Comment on the morphology of the red blood cells.
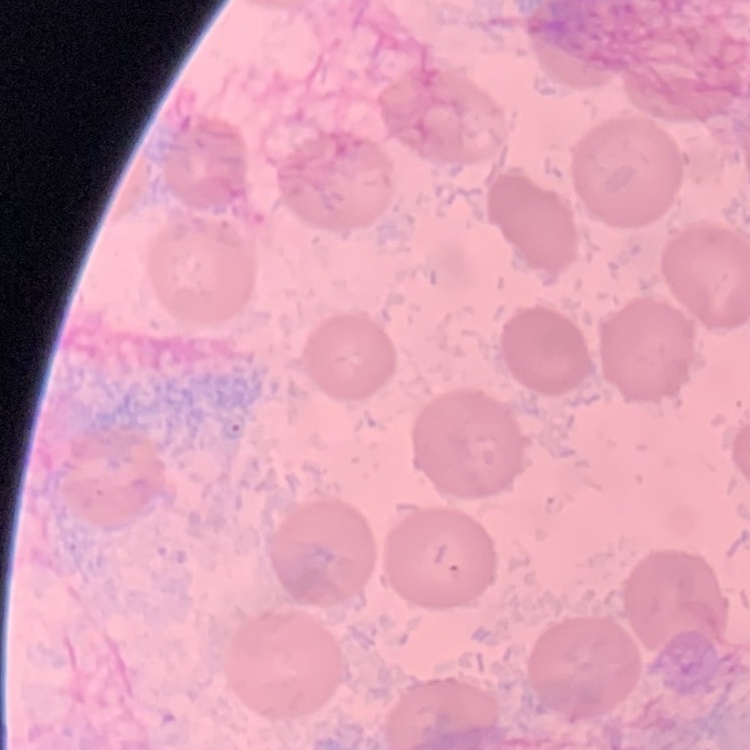
No rouleaux formation.

Summary:
  - Stain: Field's or Giemsa
  - Preparation: thin blood smear
  - Image type: one tile cut from a larger photomicrograph